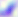
Summary:
  - Identification: Toxoplasma gondii
  - Modality: photomicrograph
  - Magnification: 400x